Assess this cell for malaria.
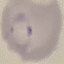
Parasitized.

preparation = thin smear
image type = cell patch, automatically extracted from a larger field of view and resized to 64 × 64 pixels
stain = Giemsa
capture = smartphone through the microscope eyepiece